Locate every leukocyte (white blood cell).
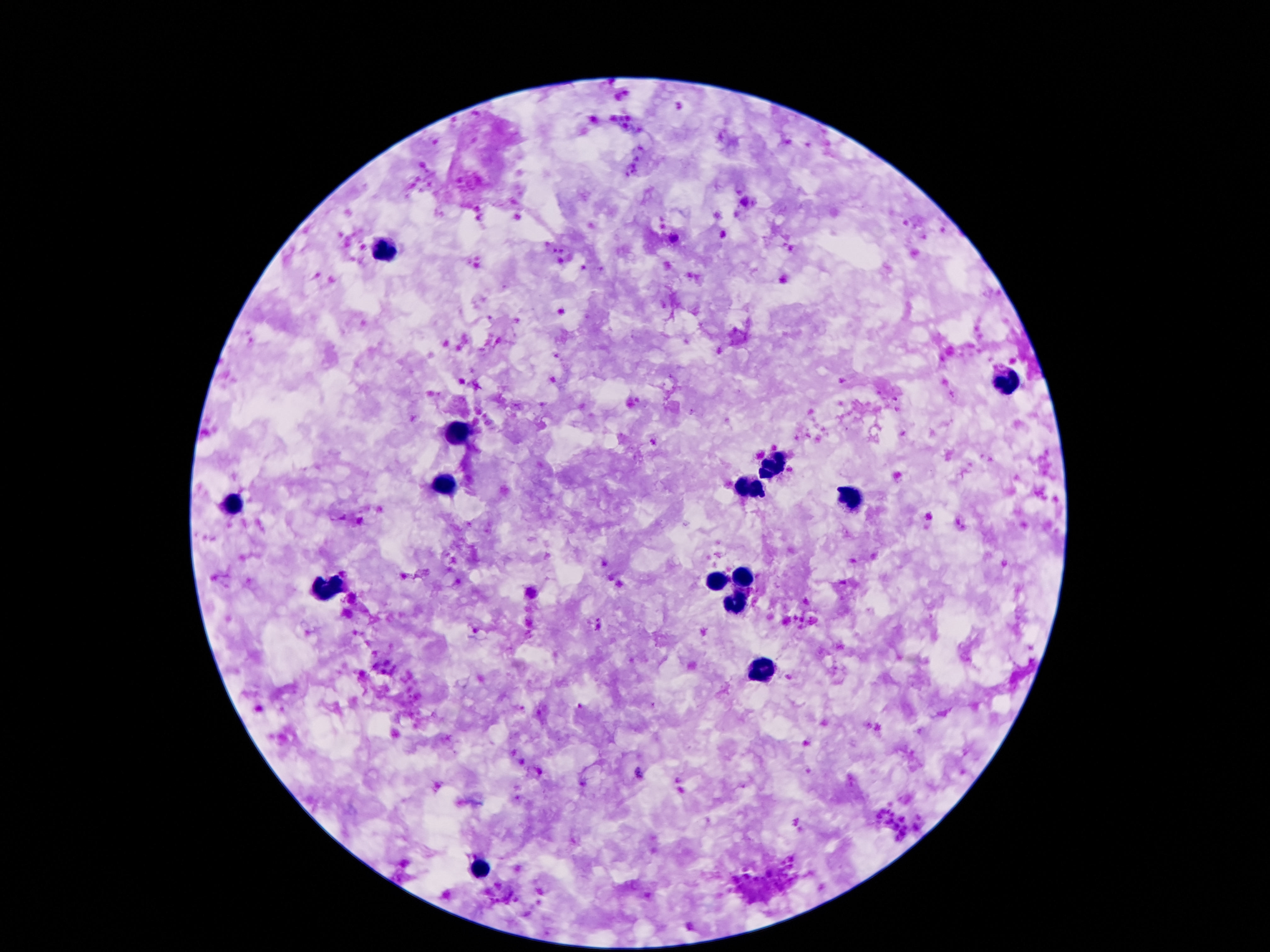

Approximate centers as [x, y] in pixels.
Leukocytes: [383, 253], [1007, 383], [458, 432], [772, 467], [441, 486], [747, 491], [851, 498], [234, 502], [743, 578], [717, 582], [323, 589], [736, 606], [764, 671], [479, 872].

Summary:
  - Capture: smartphone camera through the microscope eyepiece
  - Stain: Giemsa
  - Preparation: thick blood film
  - Patient malaria status: not infected
  - Image size: 1270×952 pixels
  - Field of view: single
  - Magnification: 100x